Locate every blood parasite and identify its species.
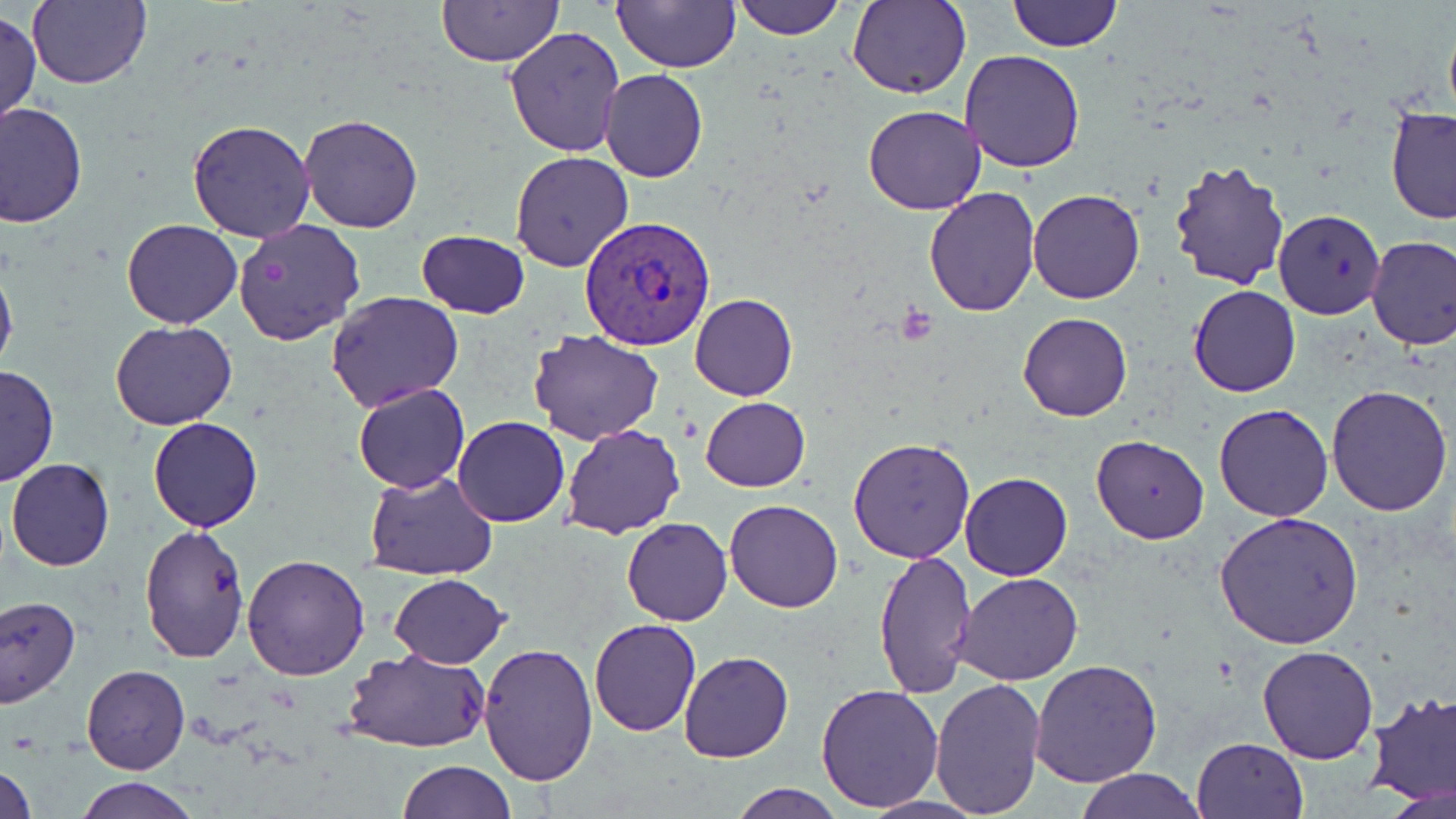

Approximate bounding boxes as (x1,y1)-(x2,y2) corner pairs in pixels.
Plasmodium vivax-infected red blood cells: (579,215)-(717,351).
No Plasmodium falciparum, Plasmodium ovale, Plasmodium malariae, Babesia divergens, or Trypanosoma brucei observed.

Uninfected red blood cell locations: (612,0)-(740,71), (733,0)-(846,40), (847,0)-(971,99), (1006,0)-(1122,52), (28,2)-(151,88), (437,2)-(563,67), (1,9)-(41,130), (1442,9)-(1456,129), (504,25)-(627,157), (959,49)-(1088,172), (599,69)-(707,182), (1,102)-(87,226), (863,104)-(987,215), (1385,106)-(1456,226), (296,113)-(424,233), (186,119)-(316,243), (509,149)-(632,276), (1168,156)-(1292,287), (923,185)-(1040,318), (1027,188)-(1145,304), (1273,210)-(1385,318), (120,219)-(244,329), (233,219)-(366,346), (414,230)-(532,318), (1366,234)-(1456,349), (0,255)-(18,381), (1190,285)-(1301,398), (327,289)-(464,411), (690,293)-(797,401), (1017,312)-(1133,422), (111,321)-(236,431), (528,329)-(663,445), (0,364)-(58,485), (353,382)-(469,493), (1327,386)-(1453,517), (700,396)-(810,491), (1214,402)-(1333,522), (453,416)-(570,527), (148,417)-(263,532), (560,424)-(686,539), (1091,434)-(1211,544), (848,438)-(975,563), (6,457)-(115,572), (364,470)-(498,579), (959,471)-(1072,580), (723,499)-(843,612), (1217,512)-(1364,651), (622,517)-(732,627), (137,525)-(250,664), (873,549)-(976,699), (241,554)-(370,682), (952,570)-(1085,685), (388,573)-(510,668), (0,594)-(80,706), (588,618)-(702,737), (476,641)-(600,785), (1258,646)-(1379,764), (342,647)-(492,752), (679,651)-(794,763), (1030,659)-(1163,789), (81,664)-(190,774), (931,675)-(1046,817), (816,683)-(945,813), (1363,689)-(1456,807), (1192,737)-(1308,819), (0,759)-(38,819), (397,759)-(514,818), (1073,769)-(1204,819), (73,777)-(200,819), (728,781)-(845,818), (857,795)-(988,819). Platelet locations: (896,303)-(938,345). Slide-level diagnosis: Plasmodium vivax. May-Grünwald-Giemsa stain. Captured at 1000x magnification. One field of a larger specimen. Image is 1456×819 pixels. Optical microscopy. Thin blood film.